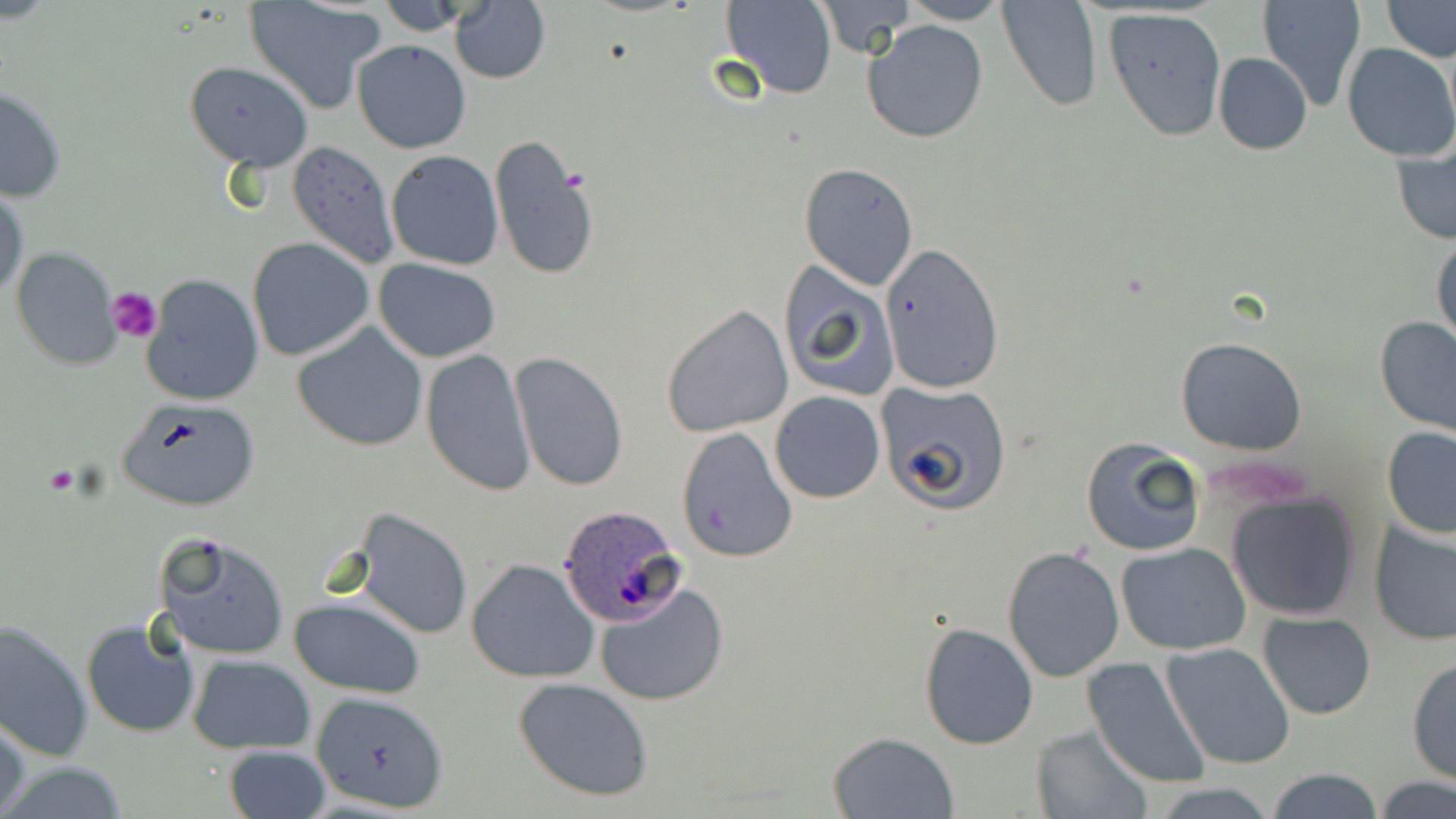

{
  "slide_level_diagnosis": "Plasmodium ovale",
  "field_of_view": "single",
  "plasmodium_ovale_infected_red_blood_cell_locations": "approximate bounding boxes as named x1/y1/x2/y2 corners in pixels: (x1=557, y1=505, x2=685, y2=627)",
  "magnification": "1000x",
  "stain": "May-Grünwald-Giemsa",
  "image_size": "1456×819 pixels",
  "preparation": "thin blood film",
  "platelet_locations": "approximate bounding boxes as named x1/y1/x2/y2 corners in pixels: (x1=107, y1=286, x2=163, y2=343)",
  "modality": "optical microscopy",
  "uninfected_red_blood_cell_locations": "approximate bounding boxes as named x1/y1/x2/y2 corners in pixels: (x1=375, y1=0, x2=480, y2=34), (x1=719, y1=0, x2=838, y2=98), (x1=898, y1=0, x2=1010, y2=24), (x1=998, y1=0, x2=1103, y2=112), (x1=1257, y1=0, x2=1368, y2=114), (x1=1380, y1=0, x2=1455, y2=61), (x1=244, y1=1, x2=383, y2=113), (x1=812, y1=1, x2=913, y2=57), (x1=449, y1=3, x2=550, y2=83), (x1=1103, y1=8, x2=1227, y2=142), (x1=863, y1=20, x2=989, y2=143), (x1=352, y1=40, x2=471, y2=153), (x1=1342, y1=43, x2=1456, y2=162), (x1=1212, y1=52, x2=1313, y2=155), (x1=185, y1=60, x2=314, y2=170), (x1=0, y1=85, x2=68, y2=202), (x1=1391, y1=135, x2=1455, y2=247), (x1=488, y1=136, x2=601, y2=284), (x1=287, y1=141, x2=400, y2=271), (x1=386, y1=150, x2=504, y2=271), (x1=799, y1=163, x2=919, y2=288), (x1=1, y1=185, x2=27, y2=305), (x1=1431, y1=230, x2=1455, y2=352), (x1=247, y1=236, x2=375, y2=361), (x1=880, y1=243, x2=1008, y2=394), (x1=10, y1=247, x2=121, y2=370), (x1=374, y1=258, x2=502, y2=363), (x1=776, y1=258, x2=900, y2=403), (x1=141, y1=273, x2=265, y2=407), (x1=661, y1=304, x2=793, y2=436), (x1=1374, y1=315, x2=1456, y2=438), (x1=293, y1=322, x2=429, y2=452), (x1=1175, y1=337, x2=1307, y2=456), (x1=420, y1=347, x2=535, y2=497), (x1=510, y1=352, x2=630, y2=491), (x1=878, y1=380, x2=1013, y2=513), (x1=769, y1=391, x2=885, y2=503), (x1=116, y1=397, x2=263, y2=512), (x1=675, y1=426, x2=798, y2=563), (x1=1382, y1=428, x2=1456, y2=541), (x1=1080, y1=438, x2=1206, y2=557), (x1=1225, y1=492, x2=1362, y2=621), (x1=350, y1=507, x2=473, y2=640), (x1=1370, y1=517, x2=1456, y2=647), (x1=158, y1=533, x2=293, y2=661), (x1=1117, y1=542, x2=1252, y2=654), (x1=1002, y1=546, x2=1125, y2=682), (x1=466, y1=559, x2=600, y2=684), (x1=594, y1=582, x2=729, y2=707), (x1=289, y1=595, x2=426, y2=700), (x1=1258, y1=610, x2=1377, y2=719), (x1=81, y1=617, x2=198, y2=739), (x1=0, y1=619, x2=94, y2=762), (x1=917, y1=623, x2=1039, y2=750), (x1=1161, y1=642, x2=1296, y2=769), (x1=186, y1=653, x2=315, y2=753), (x1=1083, y1=657, x2=1213, y2=790), (x1=1406, y1=657, x2=1455, y2=786), (x1=512, y1=676, x2=653, y2=802), (x1=310, y1=690, x2=448, y2=812), (x1=1, y1=710, x2=29, y2=819), (x1=1032, y1=726, x2=1155, y2=818), (x1=828, y1=731, x2=958, y2=817), (x1=223, y1=744, x2=331, y2=819), (x1=0, y1=760, x2=134, y2=817), (x1=1263, y1=766, x2=1387, y2=819), (x1=1370, y1=776, x2=1456, y2=819)"
}